Report the malaria status of this cell.
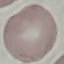
It is uninfected.

stain: Giemsa
image_type: cell patch, automatically extracted from a larger field of view and resized to 64 × 64 pixels
capture: smartphone camera at the microscope eyepiece
preparation: thin smear